Locate every Plasmodium falciparum-infected red blood cell.
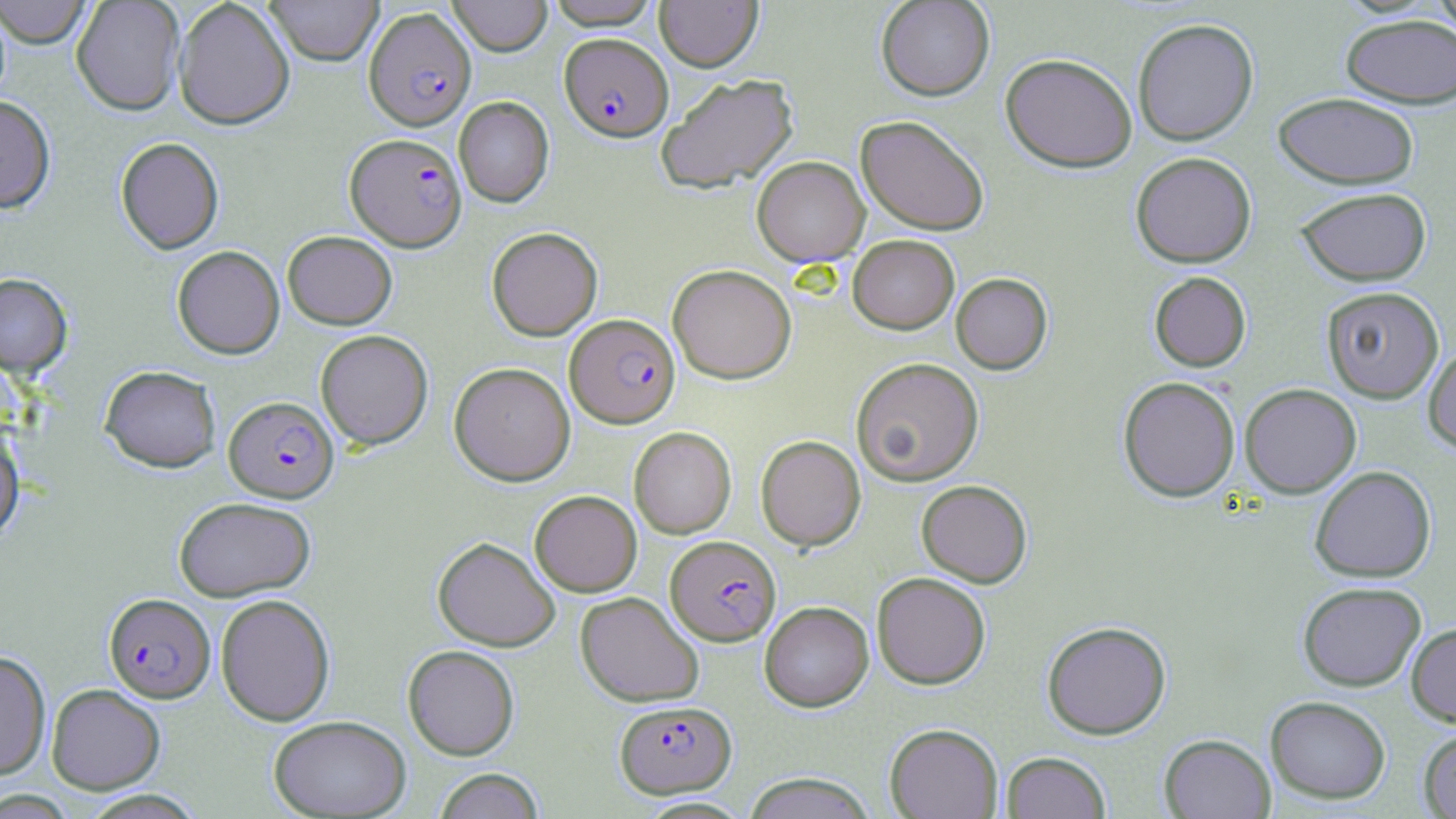

Approximate bounding boxes as (x1, y1, x2, y2) in pixels.
Plasmodium falciparum-infected red blood cells: (363, 7, 476, 130), (560, 32, 672, 141), (345, 133, 466, 251), (565, 313, 680, 428), (224, 396, 339, 502), (666, 534, 780, 645), (104, 593, 215, 703), (615, 700, 735, 798).

Summary:
  - Uninfected red blood cell locations: (1, 0, 93, 48), (71, 0, 185, 116), (173, 0, 295, 130), (265, 0, 382, 65), (447, 0, 552, 56), (546, 0, 661, 29), (654, 0, 763, 71), (876, 0, 995, 101), (1427, 0, 1456, 39), (1339, 13, 1456, 109), (1132, 18, 1258, 146), (1000, 53, 1137, 172), (655, 73, 799, 194), (1273, 92, 1419, 189), (0, 95, 56, 213), (454, 97, 554, 207), (856, 115, 990, 235), (115, 137, 223, 254), (1131, 152, 1257, 268), (752, 156, 870, 267), (1295, 187, 1432, 286), (487, 227, 603, 341), (282, 231, 397, 329), (847, 234, 959, 334), (172, 245, 285, 359), (668, 264, 796, 384), (1149, 271, 1251, 371), (0, 273, 73, 376), (951, 273, 1052, 374), (1320, 286, 1444, 403), (315, 329, 433, 449), (1424, 343, 1456, 455), (851, 357, 984, 486), (449, 362, 575, 485), (100, 365, 221, 472), (1118, 376, 1240, 502), (1239, 383, 1361, 497), (628, 426, 736, 538), (0, 427, 24, 544), (756, 435, 865, 550), (1309, 465, 1436, 582), (916, 479, 1033, 587), (530, 490, 642, 596), (174, 496, 316, 600), (433, 536, 560, 651), (871, 572, 991, 689), (1297, 581, 1426, 690), (575, 591, 704, 707), (215, 593, 335, 726), (759, 601, 874, 711), (1042, 620, 1171, 739), (1406, 622, 1456, 726), (402, 645, 520, 760), (0, 651, 51, 779), (46, 684, 165, 794), (1265, 695, 1391, 804), (268, 715, 411, 817), (884, 723, 1003, 818), (1418, 728, 1456, 818), (1159, 734, 1276, 818), (1001, 751, 1111, 819), (433, 769, 545, 819), (743, 772, 877, 818), (0, 789, 76, 817)
  - Slide-level diagnosis: Plasmodium falciparum
  - Field of view: single
  - Modality: light microscopy
  - Magnification: 1000x
  - Image size: 1456×819 pixels
  - Stain: May-Grünwald-Giemsa
  - Preparation: thin blood film